Name the cell type shown.
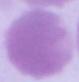
An erythrocyte.

modality = photomicrograph
magnification = 1000x